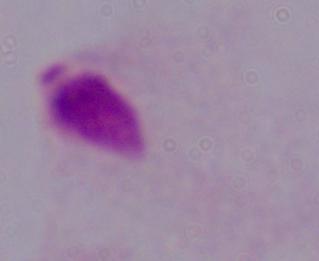

A trichomonad is shown. Captured at 1000x magnification. Photomicrograph.